Identify the parasite.
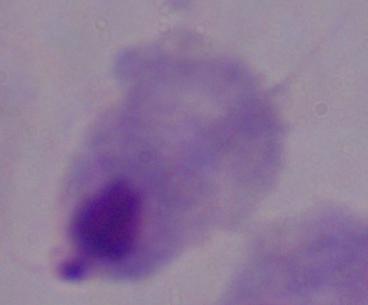
This is a trichomonad.

modality: photomicrograph
magnification: 1000x